Assess this cell for malaria.
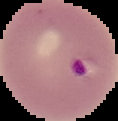

It is parasitized.

From a thin blood film. The area outside the segmented cell region is set to black. Image is 118×121 pixels.